Locate every uninfected red blood cell.
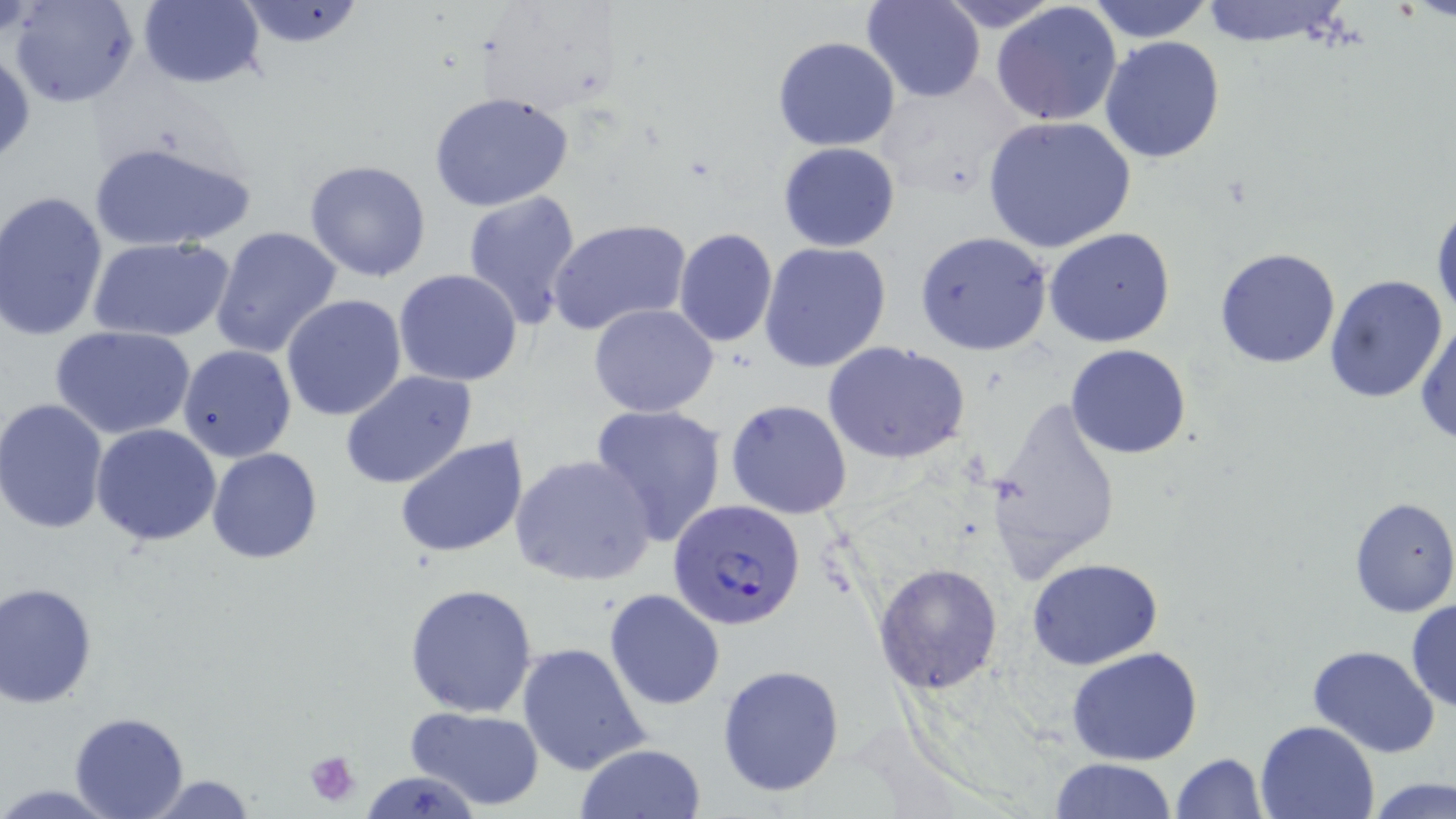

Approximate bounding boxes as (x1, y1, x2, y2) in pixels.
Uninfected red blood cells: (9, 0, 140, 108), (136, 0, 265, 89), (234, 0, 370, 51), (862, 0, 984, 103), (934, 0, 1067, 33), (1083, 0, 1215, 43), (1195, 0, 1355, 49), (991, 2, 1123, 127), (772, 37, 901, 152), (1099, 37, 1225, 163), (1, 46, 35, 166), (428, 90, 575, 211), (983, 115, 1137, 255), (89, 139, 257, 254), (778, 142, 902, 252), (304, 160, 433, 282), (461, 190, 582, 330), (1, 191, 108, 340), (1431, 198, 1455, 329), (547, 217, 691, 336), (210, 225, 343, 361), (673, 227, 778, 346), (1045, 228, 1176, 348), (914, 231, 1055, 357), (91, 239, 233, 343), (758, 242, 890, 372), (1214, 246, 1342, 369), (394, 268, 524, 386), (1324, 274, 1450, 403), (281, 294, 408, 421), (589, 303, 720, 418), (1416, 315, 1456, 447), (53, 327, 195, 440), (822, 340, 971, 465), (177, 345, 299, 463), (1065, 345, 1192, 460), (340, 371, 479, 492), (725, 398, 852, 519), (0, 399, 109, 533), (980, 400, 1123, 582), (588, 404, 729, 547), (91, 423, 222, 547), (394, 435, 529, 558), (207, 448, 323, 564), (509, 453, 655, 584), (1348, 496, 1456, 617), (1028, 557, 1164, 669), (873, 562, 1003, 695), (1, 581, 98, 707), (404, 582, 539, 719), (604, 589, 725, 711), (1406, 598, 1456, 712), (517, 641, 652, 777), (1305, 644, 1441, 758), (1065, 646, 1206, 767), (717, 664, 845, 798), (405, 705, 546, 812), (69, 713, 191, 818), (1255, 718, 1382, 818), (573, 743, 707, 819), (1169, 753, 1267, 819), (1050, 756, 1176, 818), (362, 771, 482, 818), (137, 774, 263, 816), (1366, 777, 1454, 819), (1, 783, 118, 815).

slide_level_diagnosis: Plasmodium falciparum
preparation: thin blood smear
platelet_locations: 'approximate bounding boxes as (x1, y1, x2, y2) in pixels: (304, 748, 363, 807)'
modality: light microscopy
plasmodium_falciparum_infected_red_blood_cell_locations: 'approximate bounding boxes as (x1, y1, x2, y2) in pixels: (669, 500, 805, 630)'
magnification: 1000x
image_size: 1456×819 pixels
stain: May-Grünwald-Giemsa
field_of_view: single